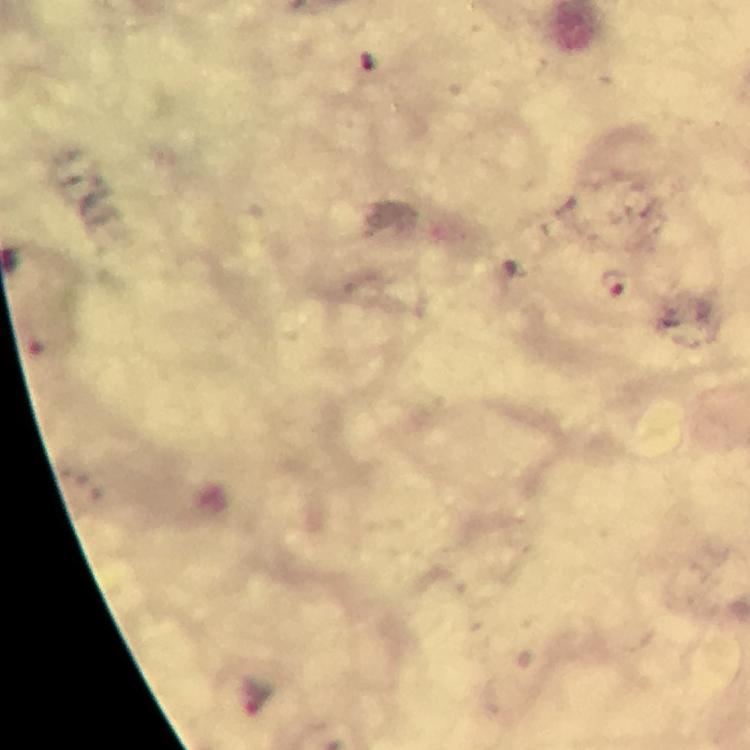

stain = Giemsa
image size = 750×750 pixels
context = from a malaria diagnostic workup
immersion oil = used
capture = smartphone photograph through a microscope
cropped from = one field of view
preparation = thick blood smear
Plasmodium parasite locations = approximate centers as (x, y) in pixels: (613, 282)
magnification = 100x